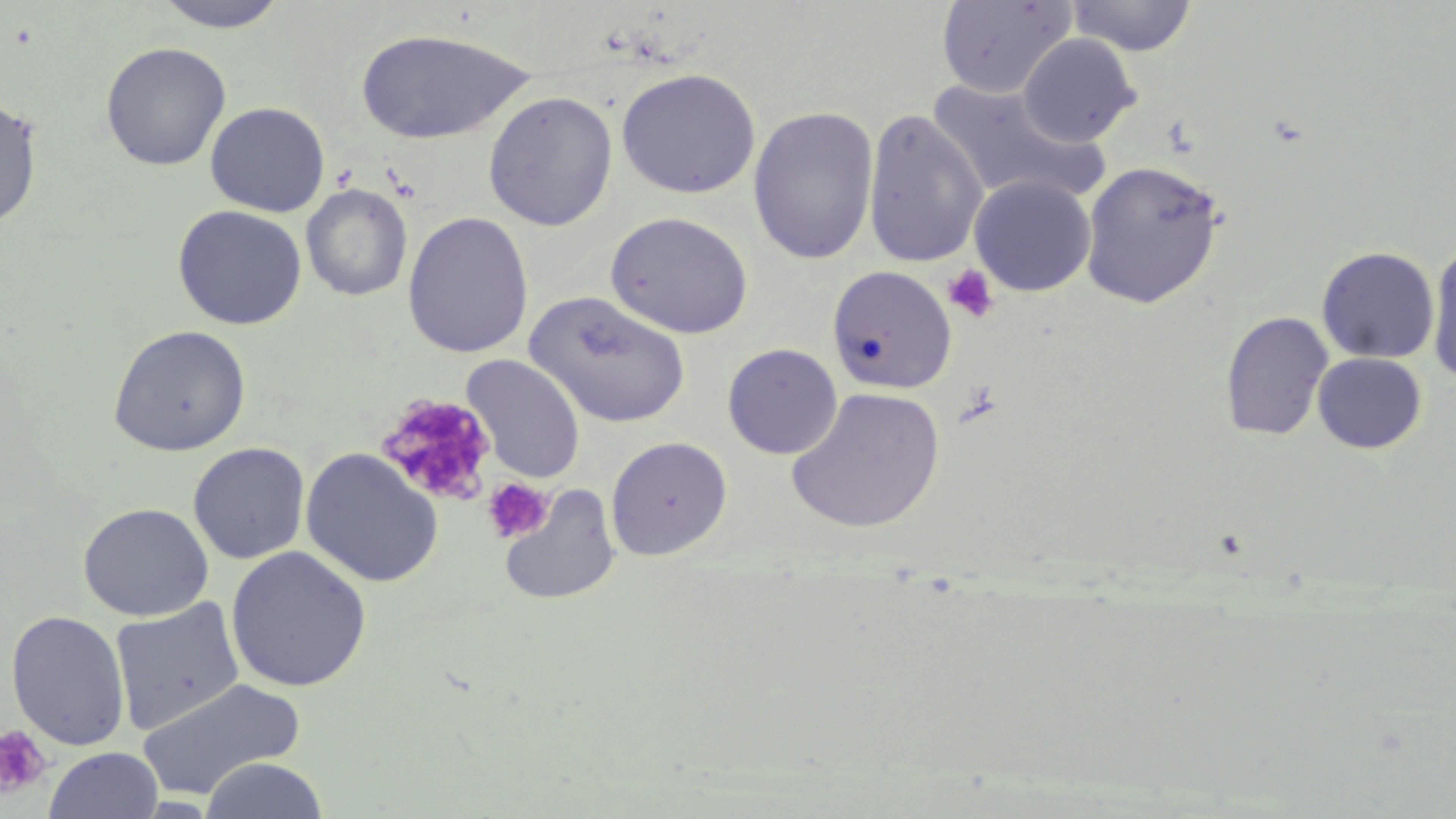 Approximate bounding boxes as named x1/y1/x2/y2 corners in pixels. Platelet locations: (x1=943, y1=264, x2=999, y2=323), (x1=378, y1=393, x2=498, y2=508), (x1=482, y1=477, x2=552, y2=543), (x1=0, y1=725, x2=53, y2=798). Uninfected red blood cell locations: (x1=150, y1=0, x2=291, y2=33), (x1=936, y1=0, x2=1077, y2=98), (x1=1065, y1=0, x2=1198, y2=56), (x1=354, y1=28, x2=531, y2=145), (x1=1017, y1=34, x2=1143, y2=146), (x1=100, y1=41, x2=232, y2=170), (x1=616, y1=68, x2=760, y2=198), (x1=925, y1=79, x2=1107, y2=208), (x1=482, y1=90, x2=618, y2=231), (x1=0, y1=97, x2=42, y2=229), (x1=205, y1=101, x2=330, y2=217), (x1=748, y1=105, x2=879, y2=265), (x1=862, y1=109, x2=988, y2=268), (x1=1079, y1=159, x2=1226, y2=309), (x1=968, y1=174, x2=1096, y2=297), (x1=300, y1=184, x2=413, y2=301), (x1=172, y1=204, x2=307, y2=330), (x1=605, y1=210, x2=753, y2=339), (x1=402, y1=211, x2=534, y2=359), (x1=1426, y1=241, x2=1456, y2=386), (x1=1317, y1=245, x2=1440, y2=364), (x1=826, y1=265, x2=957, y2=393), (x1=524, y1=291, x2=690, y2=429), (x1=1220, y1=311, x2=1334, y2=441), (x1=108, y1=324, x2=251, y2=456), (x1=722, y1=343, x2=843, y2=459), (x1=1312, y1=352, x2=1426, y2=454), (x1=461, y1=354, x2=586, y2=484), (x1=786, y1=386, x2=945, y2=534), (x1=605, y1=436, x2=732, y2=560), (x1=188, y1=442, x2=310, y2=564), (x1=300, y1=447, x2=444, y2=588), (x1=497, y1=484, x2=622, y2=606), (x1=78, y1=502, x2=214, y2=622), (x1=225, y1=546, x2=371, y2=693), (x1=109, y1=598, x2=245, y2=735), (x1=6, y1=610, x2=130, y2=750), (x1=136, y1=676, x2=307, y2=800), (x1=44, y1=747, x2=163, y2=819), (x1=199, y1=756, x2=329, y2=818). Slide-level diagnosis: negative for blood parasites. Thin blood film. Image is 1456×819 pixels. 1000x magnification. May-Grünwald-Giemsa-stained preparation. Optical microscopy. One field of a larger specimen.